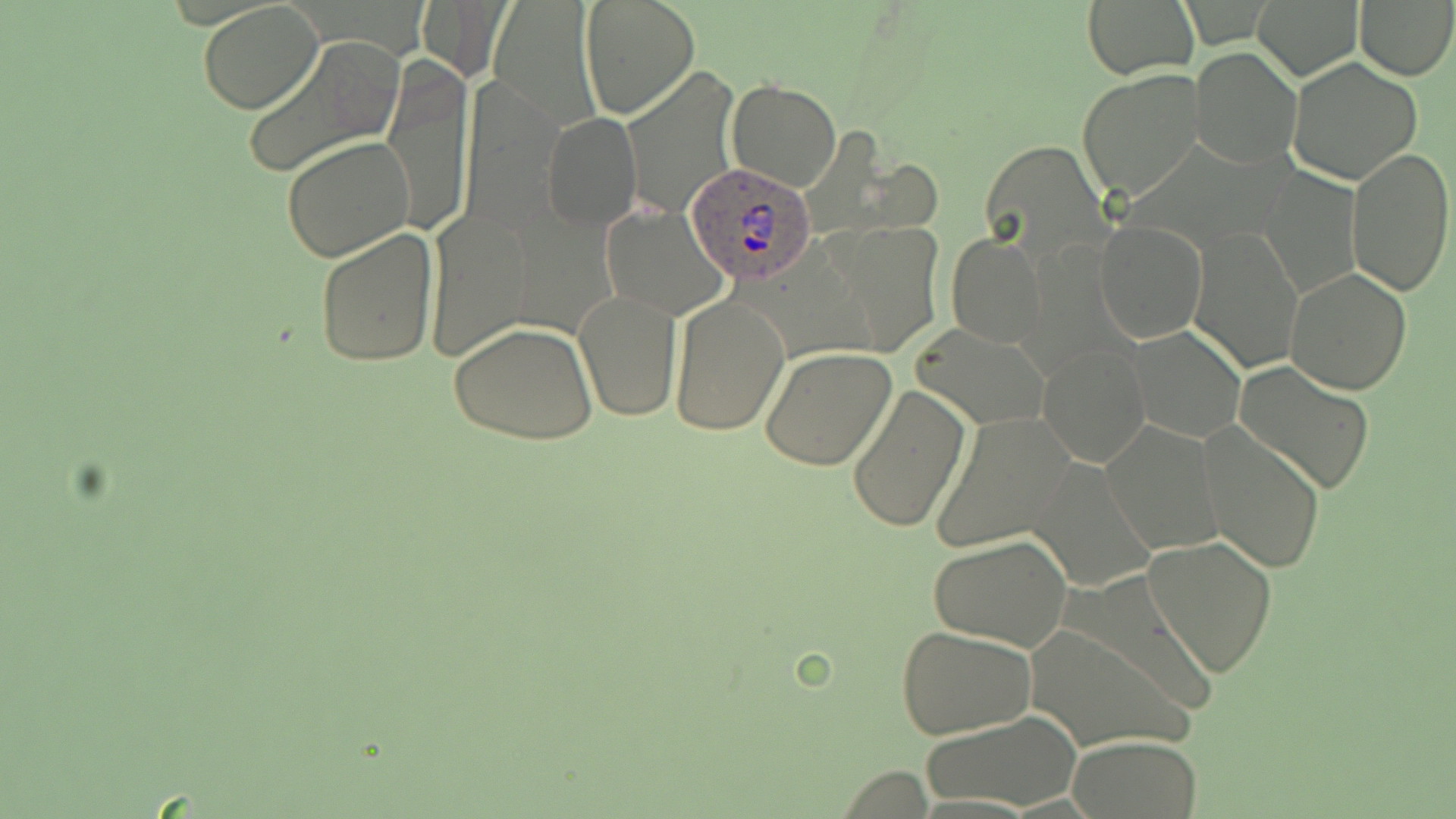
Approximate bounding boxes as (x1,y1)-(x2,y2) corner pairs in pixels. Uninfected red blood cell locations: (578,0)-(701,121), (1252,0)-(1363,81), (1354,0)-(1456,81), (415,1)-(505,79), (1083,1)-(1196,78), (197,3)-(325,114), (489,5)-(600,130), (240,37)-(404,183), (1190,47)-(1300,167), (380,55)-(476,239), (1286,57)-(1423,186), (1076,66)-(1205,203), (620,67)-(740,216), (459,78)-(563,237), (726,79)-(842,192), (541,109)-(641,231), (282,135)-(415,263), (977,137)-(1111,266), (1346,146)-(1454,297), (1261,165)-(1361,299), (601,204)-(729,319), (423,207)-(539,362), (1094,219)-(1208,343), (828,223)-(946,353), (313,226)-(437,369), (1189,226)-(1304,375), (946,233)-(1047,347), (1284,266)-(1414,394), (572,288)-(681,424), (667,292)-(789,435), (449,321)-(598,447), (914,323)-(1048,431), (1129,327)-(1245,443), (1038,341)-(1151,468), (760,346)-(897,471), (1234,363)-(1377,496), (844,379)-(968,533), (930,412)-(1077,554), (1102,421)-(1223,555), (1199,426)-(1327,575), (1027,458)-(1159,593), (1143,533)-(1278,678), (927,534)-(1072,652), (1025,617)-(1196,753), (896,625)-(1037,740), (921,712)-(1081,810), (1069,736)-(1203,817). Plasmodium ovale-infected red blood cell locations: (683,164)-(818,284). Slide-level diagnosis: Plasmodium ovale. One field of a larger specimen. Image is 1456×819 pixels. May-Grünwald-Giemsa stain. Optical microscopy. Captured at 1000x magnification. Thin blood smear.